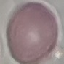 Result: no malaria parasites detected. Giemsa-stained preparation. Automatically extracted cell patch, resized to 64 × 64 pixels. Thin blood smear. Acquired by smartphone through the microscope eyepiece.